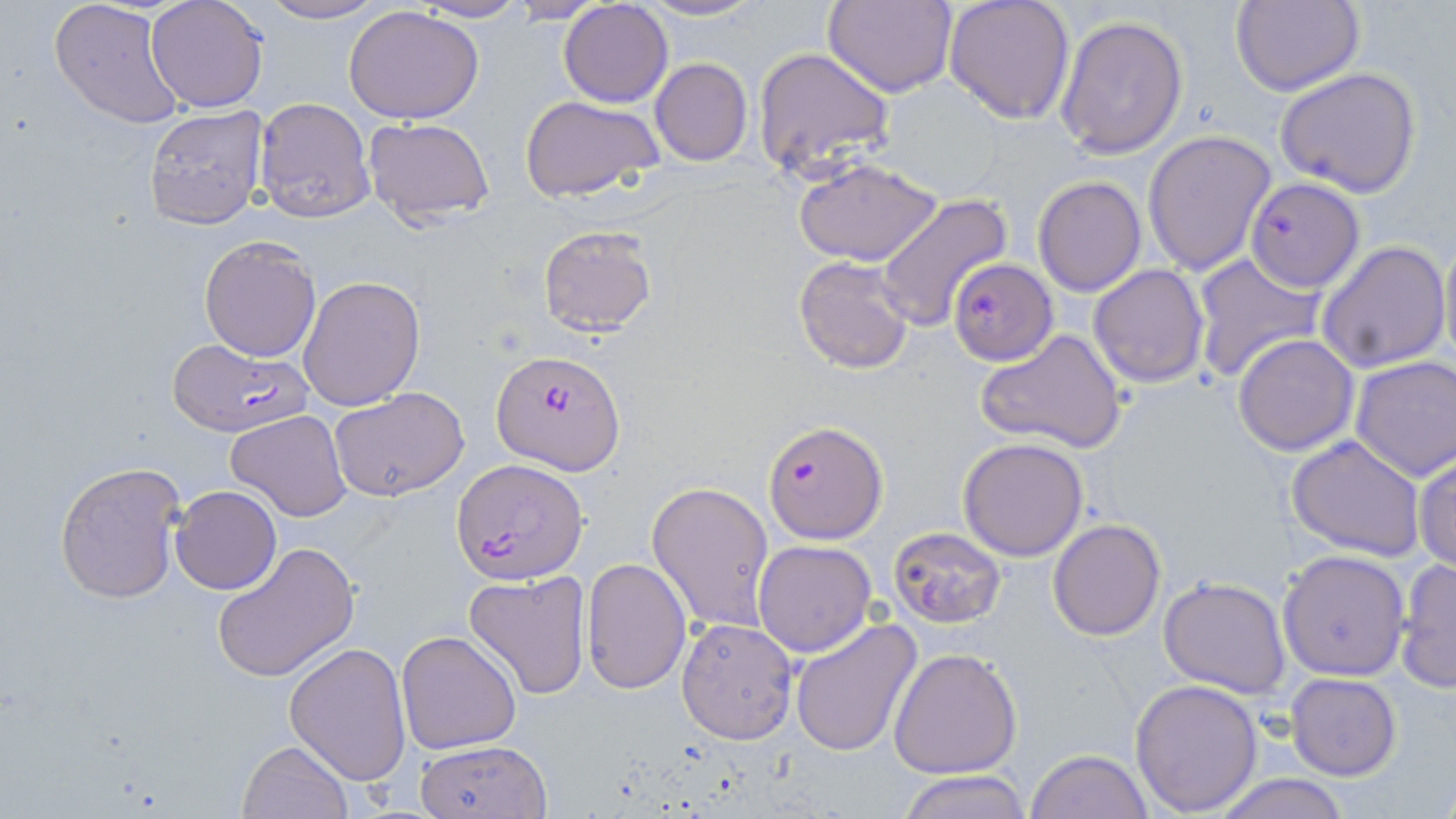
slide-level diagnosis = Plasmodium falciparum
field of view = single
modality = optical microscopy
stain = May-Grünwald-Giemsa
image size = 1456×819 pixels
magnification = 1000x
preparation = thin blood smear
uninfected red blood cell locations = approximate bounding boxes as [x1, y1, x2, y2] in pixels: [49, 0, 186, 130], [253, 0, 389, 24], [412, 0, 529, 23], [505, 0, 612, 23], [638, 0, 765, 23], [824, 0, 957, 97], [943, 0, 1076, 124], [145, 1, 269, 113], [557, 1, 673, 107], [1229, 1, 1365, 97], [343, 5, 484, 125], [1054, 15, 1190, 159], [753, 46, 896, 179], [650, 58, 753, 165], [1275, 67, 1422, 196], [518, 94, 665, 204], [254, 96, 374, 222], [142, 105, 269, 228], [363, 117, 496, 225], [1141, 129, 1276, 276], [791, 157, 944, 266], [1032, 175, 1146, 296], [874, 193, 1012, 330], [537, 225, 657, 338], [1437, 231, 1456, 378], [198, 236, 321, 362], [1316, 239, 1452, 374], [1191, 253, 1325, 382], [792, 255, 916, 375], [1088, 263, 1211, 388], [297, 275, 425, 412], [977, 329, 1128, 454], [1231, 334, 1360, 457], [1350, 355, 1456, 481], [328, 385, 469, 501], [225, 409, 352, 521], [1285, 434, 1427, 560], [957, 436, 1089, 561], [1413, 451, 1456, 572], [54, 459, 188, 604], [647, 479, 776, 634], [170, 485, 281, 594], [1048, 519, 1165, 641], [890, 526, 1007, 629], [752, 539, 877, 657], [210, 543, 358, 683], [1277, 548, 1411, 681], [1394, 557, 1455, 693], [581, 558, 692, 694], [465, 570, 593, 701], [1158, 575, 1292, 699], [675, 618, 798, 743], [791, 619, 922, 758], [396, 629, 523, 754], [286, 642, 413, 783], [888, 648, 1022, 778], [1284, 672, 1402, 781], [1128, 677, 1263, 815], [413, 738, 554, 819], [239, 740, 353, 819], [1025, 749, 1153, 819], [899, 770, 1030, 818], [1211, 773, 1354, 819]
Plasmodium falciparum-infected red blood cell locations = approximate bounding boxes as [x1, y1, x2, y2] in pixels: [1246, 176, 1365, 293], [948, 258, 1058, 364], [167, 337, 313, 437], [493, 351, 624, 471], [765, 419, 888, 542], [451, 458, 588, 585]